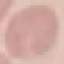 Result: no malaria parasites detected. Giemsa-stained preparation. Photographed with a smartphone camera at the microscope eyepiece. Cell patch, automatically extracted from a larger field of view and resized to 64 × 64 pixels. Thin smear of blood.